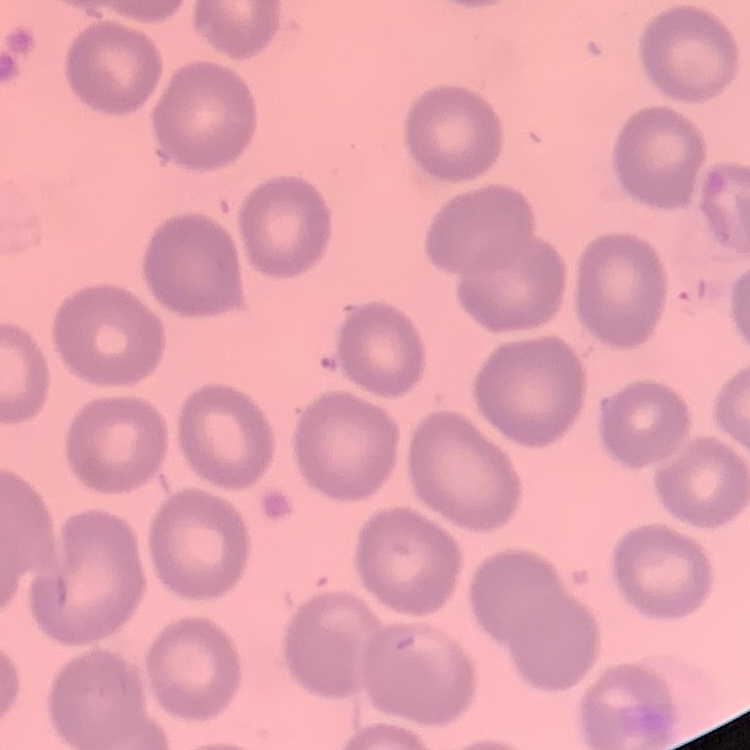

Summary:
  - Erythrocyte morphology: no rouleaux formation
  - Stain: Field's or Giemsa
  - Preparation: thin blood smear
  - Image type: one tile cut from a larger photomicrograph